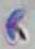
Captured at 1000x magnification. Toxoplasma gondii is seen. Photomicrograph.